Outline each Plasmodium falciparum-infected red blood cell.
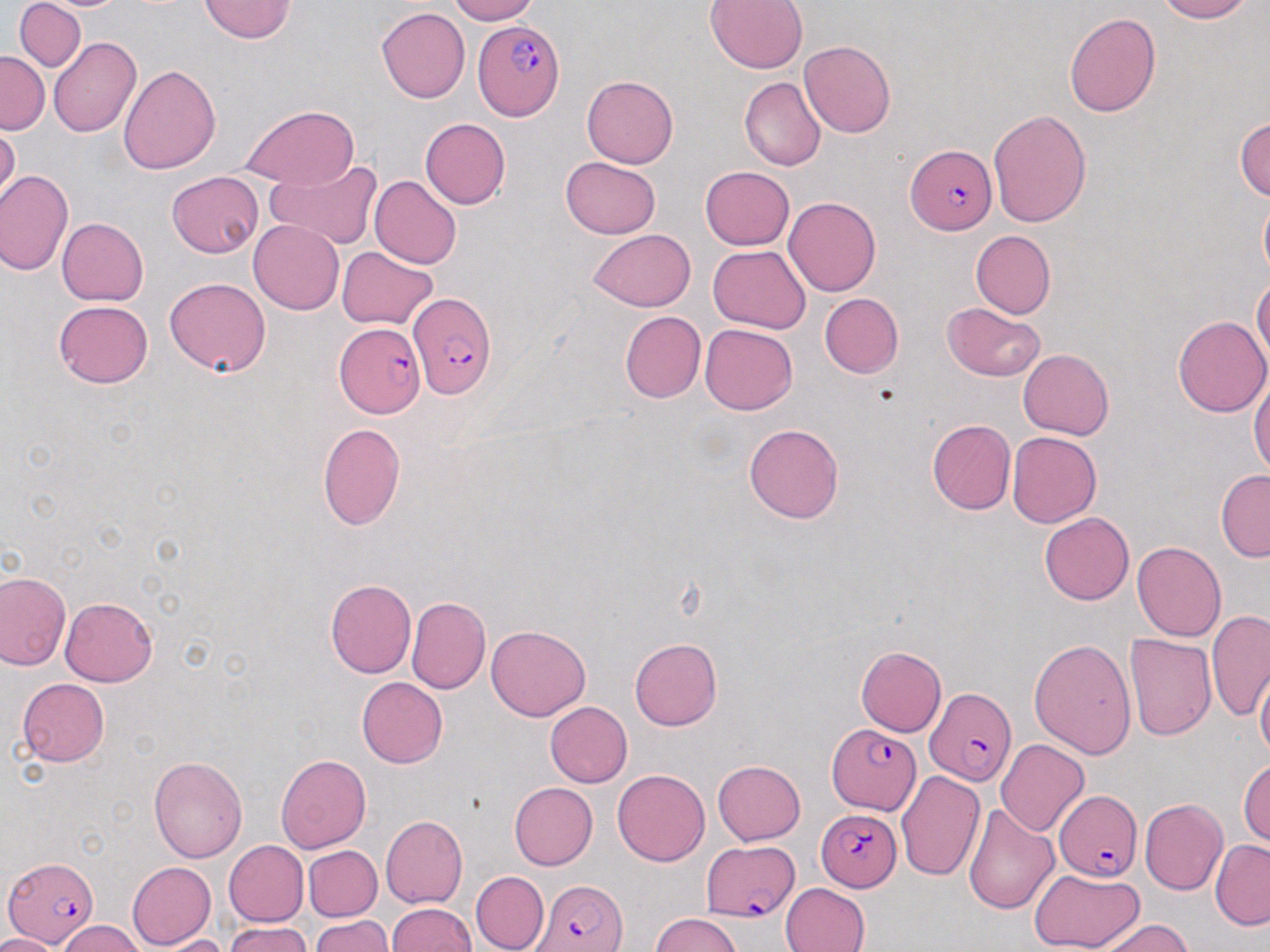
Approximate bounding boxes as (x1,y1)-(x2,y2) corner pairs in pixels.
Plasmodium falciparum-infected red blood cells: (472,19)-(565,120), (903,143)-(998,235), (407,291)-(497,398), (333,324)-(428,417), (923,688)-(1016,787), (827,722)-(923,813), (1056,790)-(1140,878), (817,808)-(904,889), (699,840)-(800,921), (3,855)-(100,945), (536,878)-(629,952).

Uninfected red blood cell locations: (200,0)-(295,43), (445,0)-(537,23), (704,0)-(807,74), (1152,0)-(1254,23), (16,1)-(88,72), (376,7)-(468,103), (1063,10)-(1163,118), (49,35)-(140,137), (798,42)-(896,138), (0,53)-(46,136), (118,63)-(220,178), (581,75)-(679,168), (740,78)-(826,171), (237,104)-(359,186), (988,107)-(1092,229), (1235,111)-(1270,210), (421,119)-(511,208), (1,125)-(20,201), (560,157)-(659,238), (265,159)-(384,249), (700,167)-(796,249), (1,169)-(74,276), (168,170)-(265,257), (371,175)-(461,269), (784,197)-(880,298), (56,216)-(148,306), (248,219)-(343,314), (586,229)-(695,310), (971,231)-(1056,317), (706,245)-(814,334), (336,246)-(440,329), (1251,270)-(1269,378), (165,278)-(270,377), (820,293)-(904,378), (54,299)-(155,389), (946,300)-(1045,380), (617,310)-(706,404), (1172,315)-(1269,417), (702,323)-(798,413), (1018,350)-(1114,438), (1250,371)-(1270,481), (317,419)-(405,532), (930,419)-(1014,514), (742,422)-(845,523), (1008,431)-(1102,526), (1217,468)-(1270,564), (1039,512)-(1133,603), (1132,540)-(1226,642), (0,571)-(71,672), (325,579)-(416,680), (60,594)-(158,685), (408,596)-(489,693), (1207,609)-(1270,718), (486,624)-(590,719), (1125,633)-(1216,741), (628,636)-(721,729), (1029,637)-(1134,758), (856,646)-(947,736), (1255,675)-(1269,762), (19,677)-(113,766), (357,677)-(447,769), (544,702)-(632,786), (995,739)-(1089,837), (148,753)-(247,864), (277,753)-(371,855), (1239,759)-(1269,846), (712,760)-(807,845), (611,769)-(709,866), (896,771)-(985,880), (509,783)-(598,869), (962,798)-(1058,915), (1139,798)-(1227,898), (381,814)-(467,906), (221,840)-(307,927), (1210,841)-(1270,929), (301,845)-(382,922), (125,861)-(214,949), (1028,869)-(1146,950), (471,871)-(548,950), (780,882)-(867,952), (387,902)-(476,952), (647,912)-(746,952), (308,915)-(391,952), (1098,916)-(1197,952), (221,922)-(312,952), (55,923)-(148,952), (0,933)-(56,952), (163,935)-(234,952). Slide-level diagnosis: Plasmodium falciparum. Thin blood smear. May-Grünwald-Giemsa stain. Image is 1270×952 pixels. One field of a larger specimen. 1000x magnification. Light microscopy.